Identify the parasite.
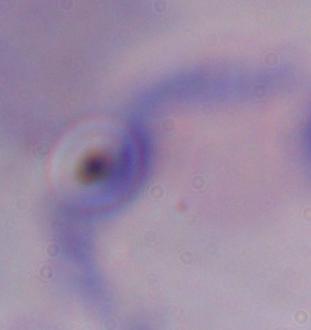
A trypanosome.

1000x magnification. Photomicrograph.